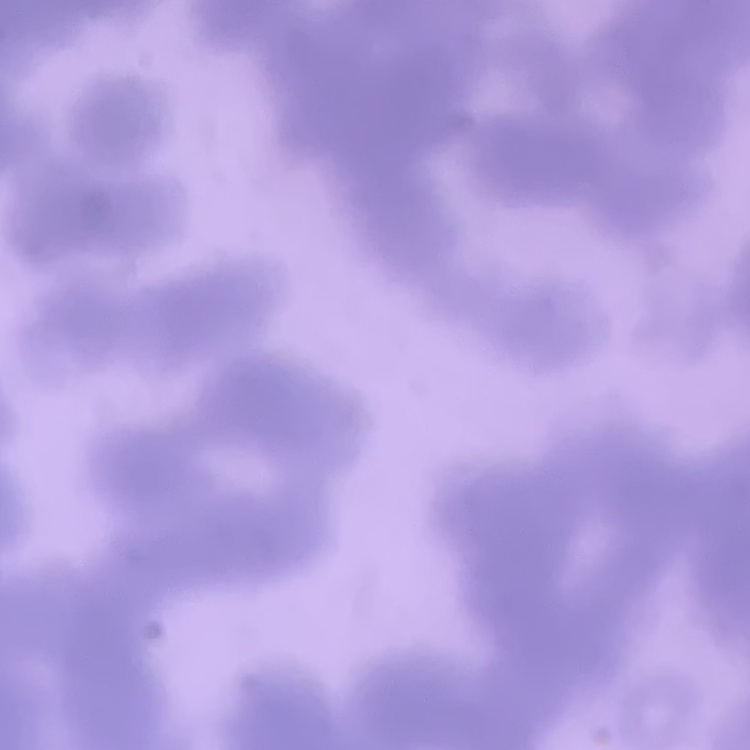

Summary:
  - Red blood cell morphology: rouleaux formation
  - Stain: Field's or Giemsa
  - Image type: square crop of a larger photomicrograph
  - Preparation: thin blood smear